Outline each Plasmodium vivax-infected red blood cell.
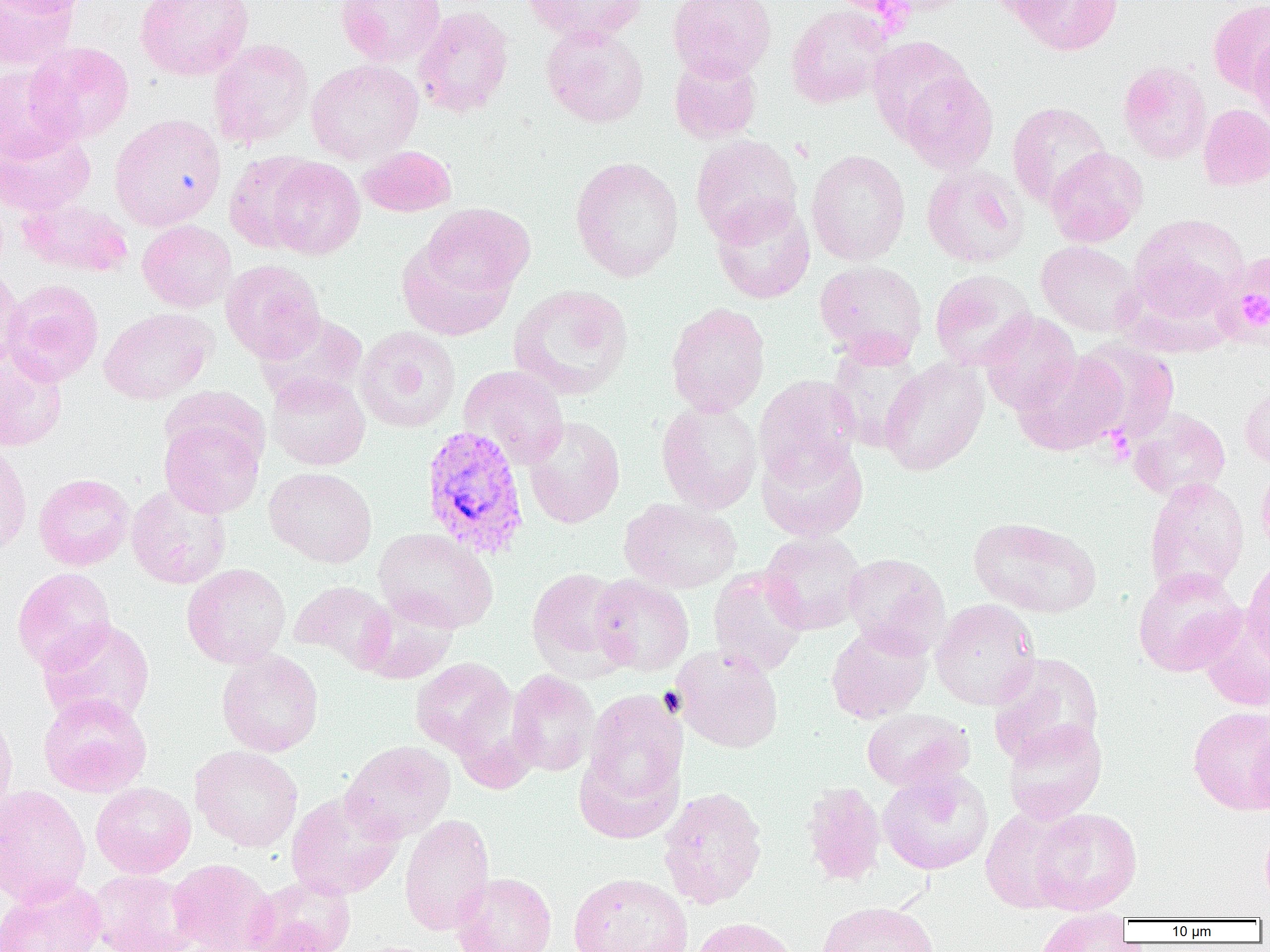

Approximate bounding boxes as (x1, y1, x2, y2) in pixels.
Plasmodium vivax-infected red blood cells: (420, 424, 531, 560).

Summary:
  - Platelet locations: (1104, 427, 1135, 465)
  - Uninfected red blood cell locations: (0, 0, 80, 70), (2, 0, 90, 17), (135, 0, 254, 81), (336, 0, 446, 66), (523, 0, 649, 45), (668, 0, 776, 81), (873, 0, 976, 16), (983, 0, 1079, 23), (1015, 0, 1124, 56), (1208, 0, 1270, 95), (785, 4, 893, 108), (414, 6, 514, 118), (541, 25, 649, 128), (1248, 35, 1270, 134), (866, 36, 974, 141), (208, 38, 313, 149), (24, 41, 134, 144), (669, 54, 762, 143), (306, 59, 424, 165), (1118, 61, 1212, 164), (0, 65, 75, 160), (897, 69, 998, 174), (1006, 102, 1111, 209), (1198, 103, 1270, 191), (110, 113, 226, 231), (0, 128, 95, 216), (690, 132, 803, 245), (359, 145, 456, 217), (1045, 147, 1148, 247), (806, 149, 911, 265), (224, 151, 319, 252), (264, 156, 365, 260), (570, 156, 684, 282), (922, 163, 1028, 268), (17, 198, 134, 278), (711, 198, 816, 304), (422, 202, 535, 299), (1129, 214, 1249, 321), (137, 220, 237, 312), (397, 239, 515, 340), (1036, 241, 1143, 336), (220, 259, 325, 362), (814, 260, 928, 364), (0, 266, 25, 372), (930, 269, 1037, 371), (2, 279, 104, 386), (508, 284, 634, 400), (665, 302, 771, 417), (99, 307, 217, 405), (978, 310, 1081, 414), (256, 312, 367, 406), (354, 325, 461, 432), (1074, 339, 1180, 443), (826, 340, 926, 450), (0, 345, 68, 451), (1012, 353, 1127, 456), (880, 358, 989, 475), (459, 365, 569, 469), (266, 372, 370, 470), (754, 375, 861, 485), (1240, 386, 1270, 469), (656, 400, 762, 514), (1129, 407, 1231, 501), (158, 410, 266, 518), (523, 416, 625, 529), (758, 439, 869, 541), (0, 442, 32, 557), (1257, 465, 1270, 561), (265, 467, 377, 567), (33, 473, 134, 571), (1144, 477, 1250, 598), (126, 484, 232, 589), (619, 498, 742, 594), (969, 516, 1101, 618), (374, 527, 498, 633), (760, 531, 867, 635), (842, 552, 950, 656), (1242, 555, 1270, 670), (182, 563, 290, 668), (708, 566, 809, 677), (11, 567, 116, 673), (527, 567, 628, 676), (1133, 567, 1246, 677), (589, 574, 694, 676), (290, 581, 396, 672), (358, 594, 460, 684), (930, 599, 1040, 710), (1198, 611, 1270, 711), (37, 618, 156, 727), (826, 623, 933, 723), (671, 644, 784, 754), (216, 650, 324, 757), (987, 652, 1104, 767), (410, 658, 517, 757), (506, 670, 599, 776), (584, 690, 687, 805), (38, 693, 152, 797), (0, 704, 17, 822), (1187, 706, 1270, 815), (861, 708, 974, 792), (1002, 719, 1107, 825), (1247, 726, 1270, 819), (341, 740, 456, 844), (190, 745, 303, 852), (574, 748, 682, 843), (878, 768, 993, 875), (91, 782, 196, 878), (800, 782, 887, 886), (0, 784, 91, 907), (658, 786, 768, 909), (286, 790, 404, 900), (980, 806, 1082, 913), (1030, 808, 1142, 914), (399, 814, 495, 936), (1259, 824, 1270, 910), (168, 858, 278, 952), (88, 869, 199, 952), (450, 872, 557, 952), (568, 872, 693, 952), (244, 875, 356, 952), (0, 876, 107, 952), (817, 901, 938, 952), (1035, 910, 1133, 952), (692, 917, 802, 952)
  - Slide-level diagnosis: Plasmodium vivax
  - Modality: light microscopy
  - Image size: 1270×952 pixels
  - Magnification: 1000x
  - Field of view: one of a larger specimen
  - Preparation: thin blood smear